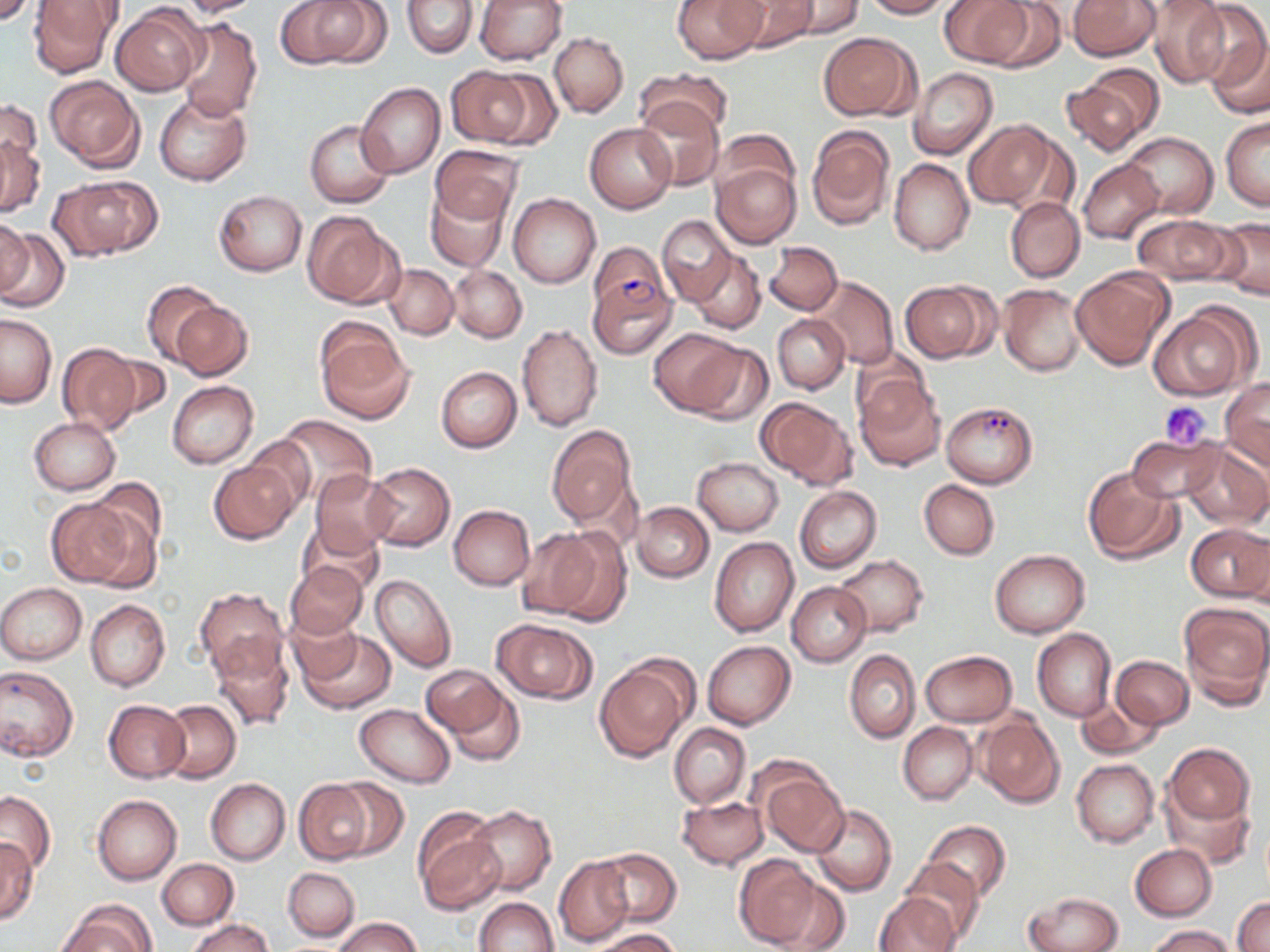

Approximate bounding boxes as (x1,y1)-(x2,y2) corner pairs in pixels. Uninfected red blood cell locations: (29,0)-(123,77), (174,0)-(263,17), (274,0)-(383,68), (475,0)-(567,64), (673,0)-(766,64), (728,0)-(816,53), (780,0)-(863,37), (862,0)-(954,18), (941,0)-(1033,68), (980,0)-(1067,71), (1068,0)-(1160,61), (1145,0)-(1230,88), (402,1)-(477,58), (1185,2)-(1270,92), (111,5)-(206,96), (174,17)-(263,122), (1205,28)-(1270,121), (819,31)-(914,120), (549,33)-(628,118), (640,66)-(732,137), (1063,66)-(1164,154), (448,67)-(540,147), (908,68)-(997,159), (44,76)-(145,171), (356,82)-(445,178), (153,92)-(251,185), (634,96)-(724,190), (0,99)-(41,183), (1221,116)-(1269,210), (963,119)-(1060,210), (305,120)-(394,208), (585,123)-(677,213), (806,126)-(894,229), (717,129)-(797,199), (0,132)-(45,219), (1122,132)-(1218,218), (430,145)-(522,227), (889,158)-(973,256), (1077,158)-(1164,244), (712,161)-(800,248), (51,175)-(160,261), (424,183)-(510,272), (213,189)-(307,276), (509,193)-(600,287), (1005,198)-(1084,281), (304,212)-(400,309), (657,214)-(736,305), (1132,215)-(1236,286), (1212,215)-(1270,301), (0,216)-(34,301), (0,224)-(68,312), (766,241)-(844,315), (588,242)-(671,324), (689,250)-(766,333), (385,264)-(458,339), (450,266)-(527,343), (1071,266)-(1172,369), (812,276)-(899,369), (142,280)-(227,366), (899,280)-(996,362), (998,284)-(1086,376), (170,300)-(254,380), (1148,306)-(1255,400), (1,313)-(56,407), (772,314)-(849,393), (316,322)-(413,425), (517,322)-(603,431), (651,329)-(746,417), (685,342)-(775,425), (56,343)-(141,434), (851,348)-(935,431), (98,354)-(173,423), (436,366)-(522,452), (854,375)-(945,471), (1221,378)-(1270,469), (167,380)-(258,469), (756,397)-(856,488), (271,414)-(377,506), (29,417)-(120,494), (546,426)-(637,527), (1127,433)-(1225,504), (238,434)-(320,514), (1181,440)-(1269,529), (692,457)-(783,535), (208,460)-(299,545), (363,463)-(454,550), (1083,466)-(1185,565), (311,468)-(396,560), (919,479)-(1000,560), (76,483)-(162,580), (794,486)-(881,573), (46,496)-(138,588), (631,502)-(712,583), (448,505)-(535,590), (302,523)-(384,595), (1186,525)-(1270,603), (515,527)-(613,621), (709,537)-(799,637), (989,549)-(1090,637), (835,554)-(930,637), (284,560)-(368,639), (371,572)-(457,672), (787,582)-(871,666), (0,583)-(86,664), (195,588)-(289,679), (85,600)-(170,692), (1179,603)-(1270,705), (289,614)-(363,683), (493,619)-(597,703), (295,628)-(395,714), (1033,628)-(1117,722), (210,636)-(294,732), (703,640)-(795,729), (844,650)-(920,743), (920,650)-(1017,727), (1111,656)-(1193,728), (422,663)-(523,759), (594,663)-(687,762), (0,664)-(79,762), (1075,698)-(1162,760), (104,700)-(189,782), (160,701)-(241,782), (354,703)-(455,787), (975,714)-(1064,807), (898,722)-(977,804), (669,723)-(751,809), (1165,743)-(1254,825), (1072,759)-(1159,848), (757,767)-(850,856), (330,776)-(408,861), (205,778)-(290,864), (293,779)-(379,864), (1162,788)-(1254,868), (0,791)-(55,875), (92,794)-(181,885), (677,796)-(769,870), (810,805)-(896,897), (466,806)-(557,895), (413,813)-(505,914), (923,820)-(1010,903), (1,838)-(37,923), (1129,844)-(1217,921), (595,848)-(680,927), (733,854)-(823,949), (553,855)-(634,947), (899,857)-(985,943), (156,858)-(238,930), (283,866)-(360,941), (771,872)-(853,952), (1025,891)-(1124,952), (874,893)-(960,952), (1233,896)-(1270,952), (474,897)-(558,951), (56,902)-(153,952), (332,917)-(423,952), (186,918)-(277,952), (1147,926)-(1235,952), (595,928)-(684,951). Plasmodium falciparum-infected red blood cell locations: (589,276)-(677,359), (941,401)-(1038,488). Platelet locations: (1159,401)-(1213,449). Slide-level diagnosis: Plasmodium falciparum. One field of a larger specimen. May-Grünwald-Giemsa stain. Light microscopy. Captured at 1000x magnification. Thin blood smear. Image is 1270×952 pixels.